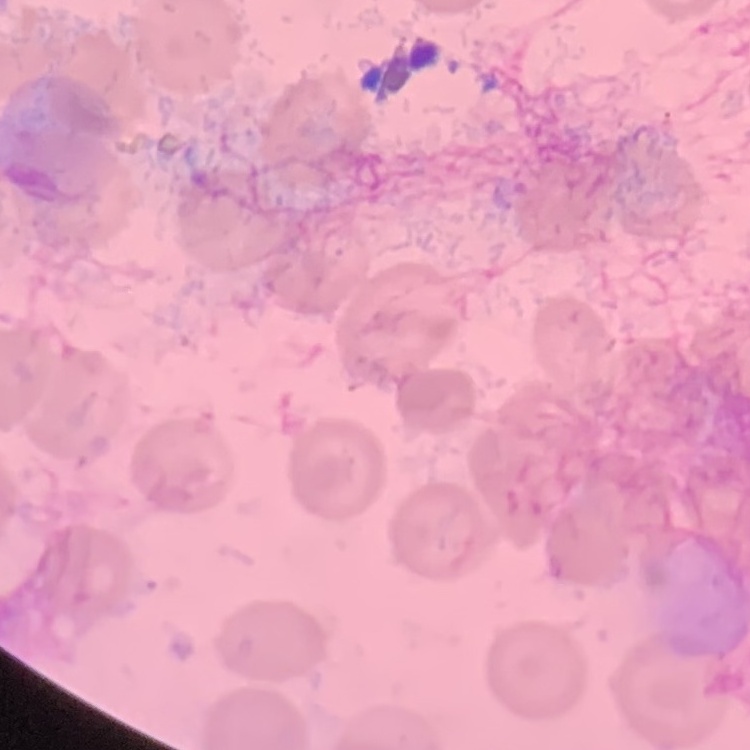

erythrocyte morphology = no rouleaux formation
preparation = thin blood smear
stain = Field's or Giemsa
image type = one tile cut from a larger photomicrograph